Give the position of every malaria parasite.
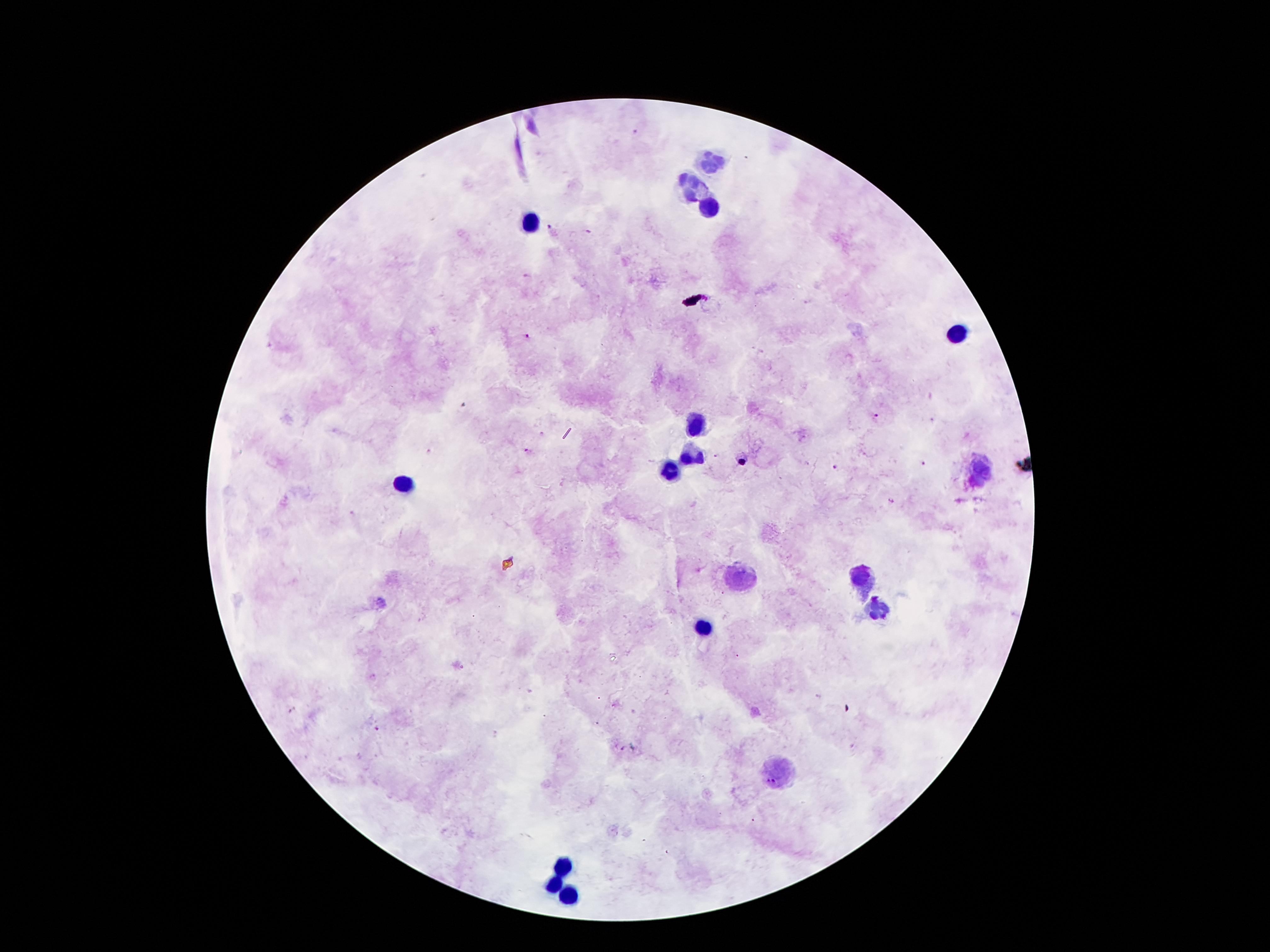
Approximate object centers, in pixels from the top-left corner.
Malaria parasites: (x=634, y=131), (x=553, y=228), (x=528, y=277), (x=810, y=303), (x=528, y=338), (x=876, y=415), (x=930, y=419), (x=528, y=450), (x=428, y=451), (x=717, y=456), (x=742, y=462), (x=923, y=464), (x=836, y=467), (x=891, y=501), (x=353, y=513), (x=373, y=676), (x=293, y=712), (x=376, y=729), (x=624, y=747).

Leukocyte locations: (x=710, y=162), (x=692, y=185), (x=706, y=205), (x=528, y=221), (x=955, y=337), (x=698, y=426), (x=690, y=455), (x=673, y=469), (x=983, y=478), (x=406, y=483), (x=862, y=576), (x=740, y=580), (x=878, y=608), (x=703, y=628), (x=780, y=771), (x=563, y=864), (x=555, y=882), (x=565, y=894). Image is 1270×952 pixels. Giemsa stain. Thick peripheral-blood smear. Patient malaria status: positive for Plasmodium falciparum. 100x magnification. Smartphone photograph taken through the microscope eyepiece. One field from this slide.